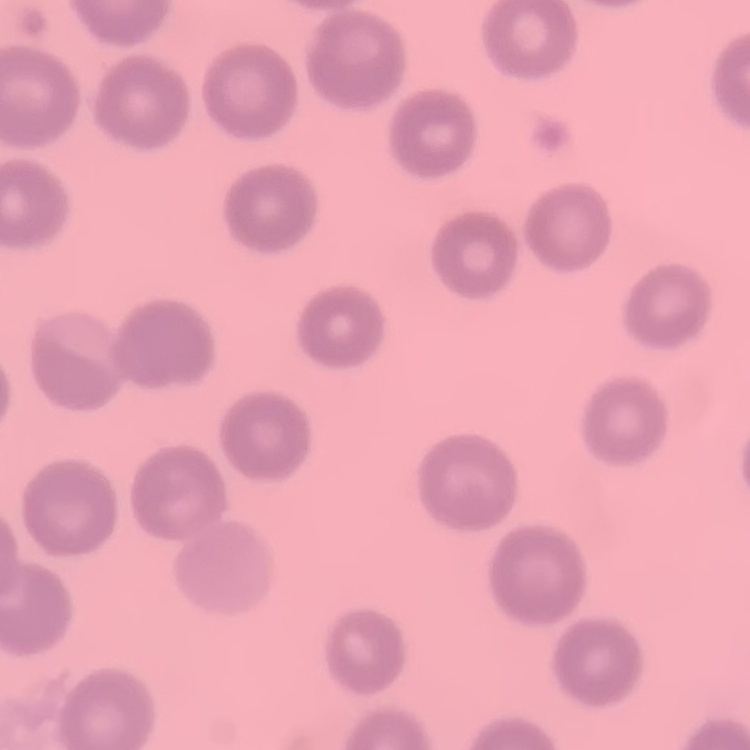 The red blood cells exhibit no rouleaux formation. One tile cut from a larger photomicrograph. Field's or Giemsa stain. Thin peripheral smear.